Assess this cell for malaria.
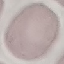

It is uninfected.

Automatically extracted cell patch, resized to 64 × 64 pixels. Photographed with a smartphone camera at the microscope eyepiece. Giemsa-stained preparation. Thin blood smear.